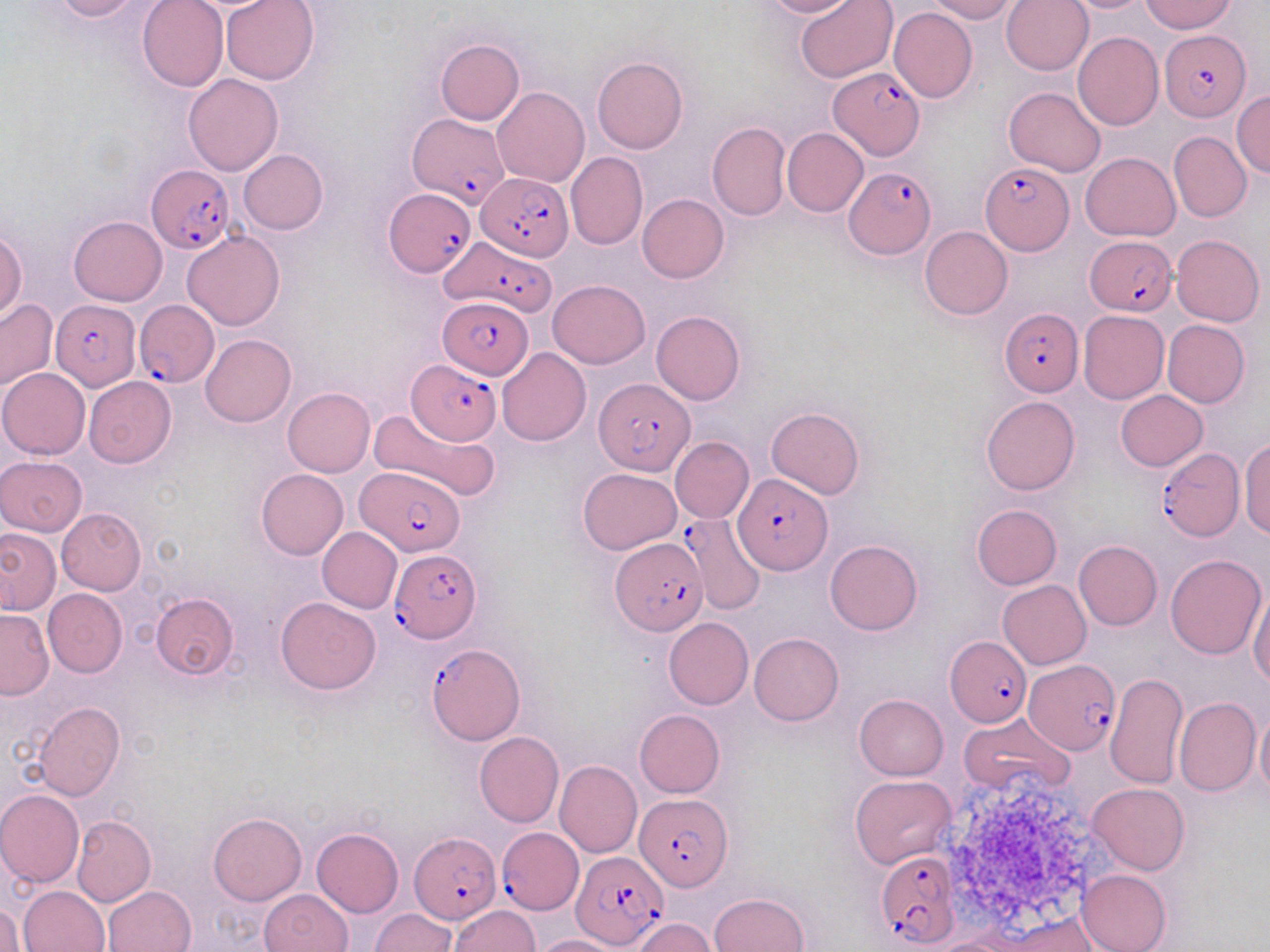
Summary:
  - Coordinate format: approximate bounding boxes as named x1/y1/x2/y2 corners in pixels
  - Uninfected red blood cell locations: (x1=50, y1=0, x2=150, y2=22), (x1=137, y1=0, x2=228, y2=92), (x1=220, y1=0, x2=321, y2=85), (x1=759, y1=0, x2=859, y2=19), (x1=794, y1=0, x2=899, y2=84), (x1=927, y1=0, x2=1019, y2=22), (x1=1001, y1=0, x2=1093, y2=75), (x1=1059, y1=0, x2=1155, y2=13), (x1=1140, y1=0, x2=1236, y2=34), (x1=889, y1=7, x2=977, y2=102), (x1=1073, y1=32, x2=1162, y2=131), (x1=435, y1=38, x2=524, y2=125), (x1=592, y1=56, x2=687, y2=154), (x1=182, y1=72, x2=283, y2=175), (x1=1004, y1=86, x2=1108, y2=177), (x1=493, y1=87, x2=589, y2=187), (x1=1232, y1=89, x2=1270, y2=178), (x1=708, y1=121, x2=791, y2=220), (x1=782, y1=128, x2=868, y2=216), (x1=1169, y1=132, x2=1251, y2=223), (x1=239, y1=150, x2=328, y2=235), (x1=566, y1=152, x2=648, y2=250), (x1=1080, y1=152, x2=1181, y2=241), (x1=637, y1=194, x2=729, y2=282), (x1=69, y1=216, x2=167, y2=306), (x1=919, y1=226, x2=1012, y2=320), (x1=0, y1=229, x2=26, y2=321), (x1=182, y1=231, x2=284, y2=330), (x1=1171, y1=234, x2=1265, y2=326), (x1=548, y1=278, x2=649, y2=369), (x1=0, y1=299, x2=57, y2=391), (x1=1078, y1=310, x2=1169, y2=403), (x1=651, y1=311, x2=745, y2=405), (x1=1162, y1=319, x2=1250, y2=407), (x1=200, y1=334, x2=296, y2=427), (x1=498, y1=348, x2=591, y2=447), (x1=0, y1=367, x2=90, y2=459), (x1=84, y1=377, x2=176, y2=468), (x1=282, y1=388, x2=375, y2=477), (x1=1115, y1=390, x2=1208, y2=470), (x1=981, y1=395, x2=1079, y2=495), (x1=369, y1=406, x2=500, y2=505), (x1=766, y1=406, x2=864, y2=500), (x1=670, y1=436, x2=754, y2=524), (x1=1239, y1=438, x2=1270, y2=539), (x1=0, y1=456, x2=88, y2=535), (x1=578, y1=467, x2=683, y2=555), (x1=256, y1=469, x2=349, y2=559), (x1=971, y1=504, x2=1061, y2=590), (x1=57, y1=508, x2=145, y2=594), (x1=317, y1=527, x2=402, y2=612), (x1=0, y1=528, x2=60, y2=614), (x1=825, y1=539, x2=923, y2=636), (x1=1073, y1=540, x2=1161, y2=630), (x1=1165, y1=554, x2=1266, y2=660), (x1=997, y1=580, x2=1091, y2=669), (x1=1248, y1=581, x2=1270, y2=688), (x1=42, y1=588, x2=127, y2=677), (x1=151, y1=592, x2=240, y2=679), (x1=275, y1=596, x2=381, y2=694), (x1=0, y1=609, x2=53, y2=699), (x1=664, y1=617, x2=754, y2=710), (x1=749, y1=632, x2=843, y2=725), (x1=1106, y1=671, x2=1188, y2=789), (x1=854, y1=694, x2=948, y2=780), (x1=1174, y1=697, x2=1259, y2=797), (x1=33, y1=702, x2=124, y2=800), (x1=1255, y1=702, x2=1270, y2=797), (x1=634, y1=709, x2=724, y2=798), (x1=960, y1=712, x2=1075, y2=796), (x1=474, y1=731, x2=563, y2=827), (x1=554, y1=760, x2=642, y2=858), (x1=849, y1=774, x2=957, y2=868), (x1=1087, y1=783, x2=1189, y2=875), (x1=0, y1=789, x2=84, y2=888), (x1=209, y1=812, x2=307, y2=905), (x1=72, y1=815, x2=155, y2=907), (x1=311, y1=827, x2=403, y2=917), (x1=1076, y1=869, x2=1171, y2=952), (x1=19, y1=884, x2=110, y2=951), (x1=103, y1=886, x2=195, y2=952), (x1=260, y1=889, x2=353, y2=952), (x1=710, y1=892, x2=808, y2=952), (x1=1, y1=902, x2=23, y2=952), (x1=449, y1=905, x2=539, y2=952), (x1=370, y1=908, x2=455, y2=952), (x1=630, y1=917, x2=716, y2=952), (x1=984, y1=917, x2=1108, y2=952), (x1=533, y1=935, x2=627, y2=952)
  - Plasmodium falciparum-infected red blood cell locations: (x1=1158, y1=30, x2=1250, y2=119), (x1=828, y1=67, x2=925, y2=160), (x1=407, y1=112, x2=509, y2=209), (x1=979, y1=161, x2=1073, y2=255), (x1=842, y1=166, x2=936, y2=259), (x1=145, y1=167, x2=234, y2=253), (x1=474, y1=172, x2=572, y2=260), (x1=384, y1=190, x2=473, y2=277), (x1=439, y1=234, x2=557, y2=315), (x1=1085, y1=234, x2=1176, y2=316), (x1=51, y1=297, x2=142, y2=393), (x1=438, y1=298, x2=534, y2=379), (x1=134, y1=300, x2=220, y2=388), (x1=1000, y1=309, x2=1083, y2=397), (x1=407, y1=361, x2=502, y2=442), (x1=594, y1=376, x2=697, y2=477), (x1=1155, y1=448, x2=1244, y2=541), (x1=354, y1=466, x2=466, y2=556), (x1=734, y1=474, x2=831, y2=576), (x1=651, y1=520, x2=759, y2=622), (x1=612, y1=537, x2=707, y2=636), (x1=390, y1=548, x2=481, y2=641), (x1=945, y1=636, x2=1033, y2=726), (x1=426, y1=643, x2=526, y2=744), (x1=1024, y1=658, x2=1121, y2=755), (x1=634, y1=792, x2=731, y2=891), (x1=496, y1=827, x2=582, y2=913), (x1=410, y1=831, x2=500, y2=923), (x1=873, y1=849, x2=962, y2=948), (x1=572, y1=851, x2=667, y2=948)
  - Slide-level diagnosis: Plasmodium falciparum
  - Magnification: 1000x
  - Preparation: thin blood film
  - Modality: light microscopy
  - Image size: 1270×952 pixels
  - Stain: May-Grünwald-Giemsa
  - Field of view: single